Give the position of every leukocyte visible.
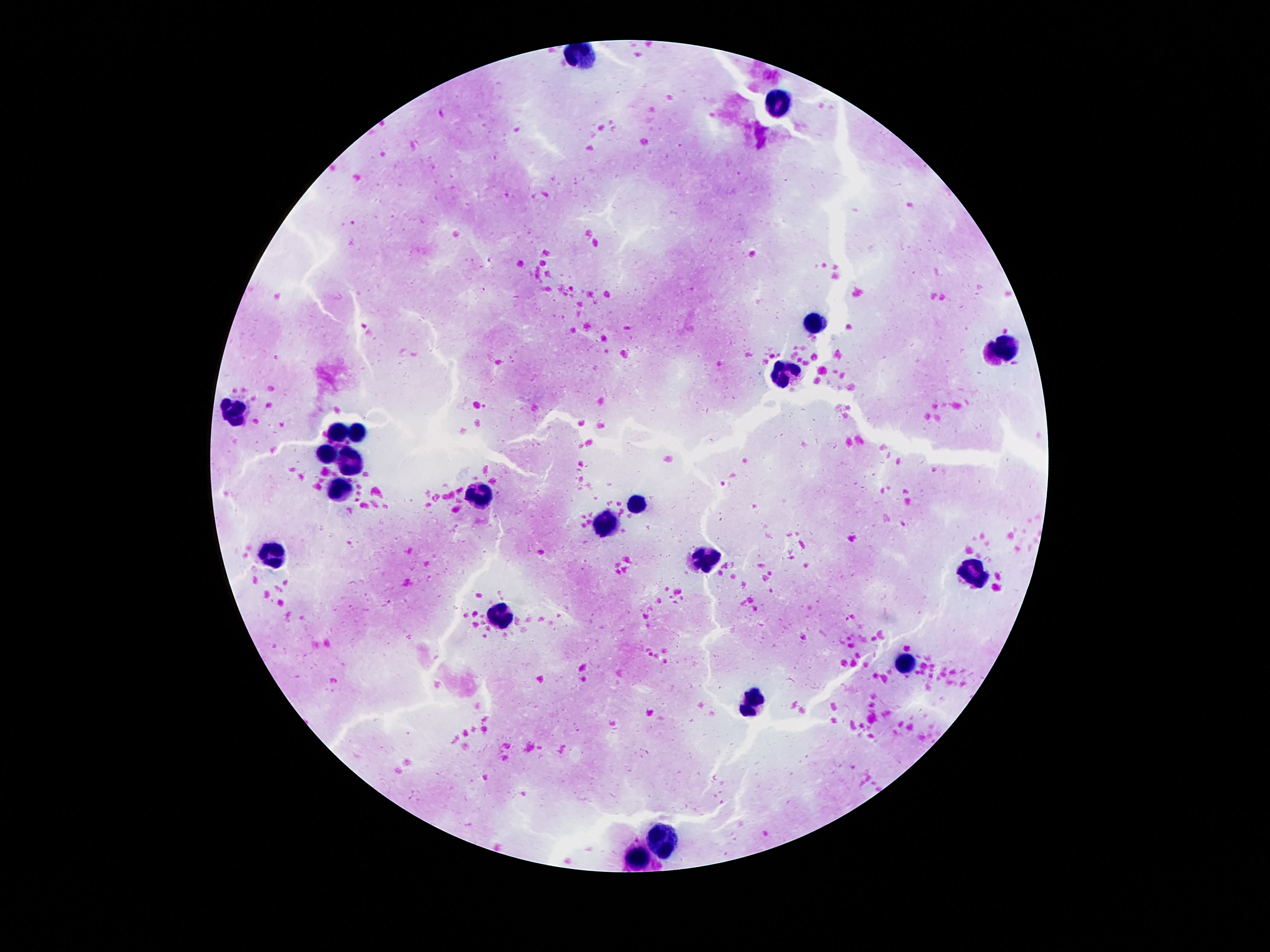

Approximate object centers, in pixels from the top-left corner.
Leukocytes: (x=581, y=56), (x=776, y=104), (x=817, y=320), (x=1005, y=347), (x=785, y=372), (x=232, y=410), (x=358, y=431), (x=336, y=433), (x=325, y=456), (x=349, y=462), (x=341, y=488), (x=479, y=493), (x=636, y=501), (x=606, y=524), (x=274, y=553), (x=706, y=561), (x=969, y=571), (x=501, y=615), (x=906, y=660), (x=753, y=701), (x=660, y=835), (x=636, y=860).

image_size: 1270×952 pixels
capture: smartphone camera through the microscope eyepiece
magnification: 100x
patient_malaria_status: negative
stain: Giemsa
preparation: thick peripheral-blood smear
field_of_view: single